Comment on the morphology of the erythrocytes.
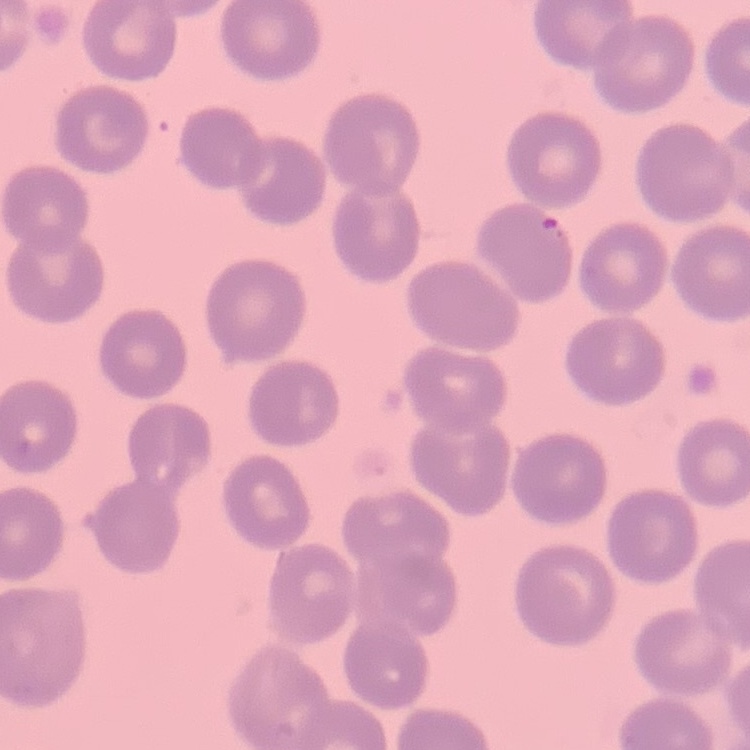
They show no rouleaux formation.

image_type: one tile cut from a larger photomicrograph
stain: Field's or Giemsa
preparation: thin peripheral smear